Locate leukocytes (white blood cells).
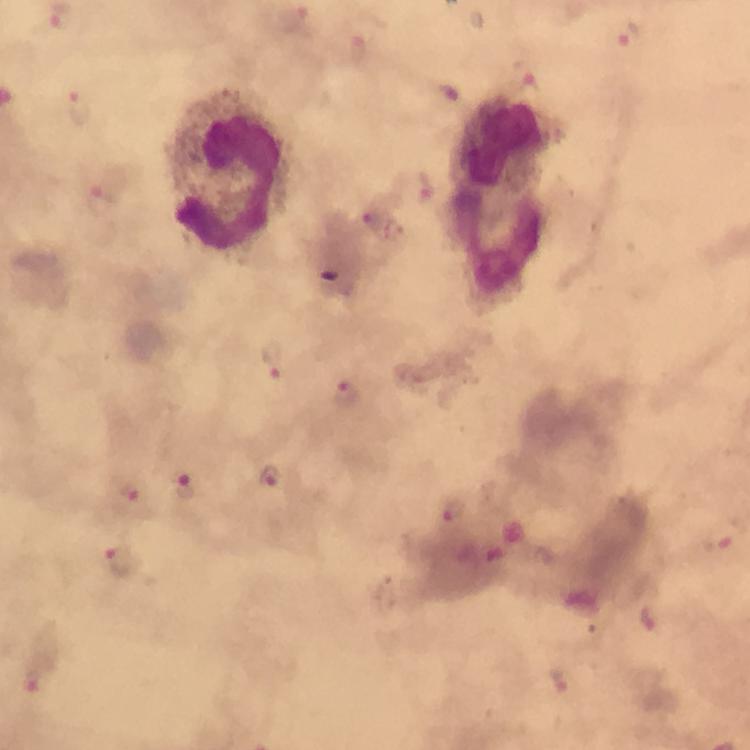
Approximate object centers, in pixels from the top-left corner.
Leukocytes: (x=503, y=140), (x=231, y=175), (x=498, y=247).

immersion oil = used
stain = Giemsa
context = from a malaria diagnostic workup
image size = 750×750 pixels
preparation = thick smear
cropped from = a single field of view
Plasmodium parasite locations = approximate object centers, in pixels from the top-left corner: (x=630, y=36), (x=355, y=47), (x=526, y=83), (x=78, y=106), (x=425, y=189), (x=99, y=200), (x=367, y=217), (x=393, y=231), (x=274, y=361), (x=346, y=392), (x=270, y=477), (x=185, y=486), (x=132, y=495), (x=451, y=509), (x=724, y=536), (x=121, y=562), (x=648, y=618), (x=31, y=681)
capture = smartphone mounted on the microscope
magnification = 100x